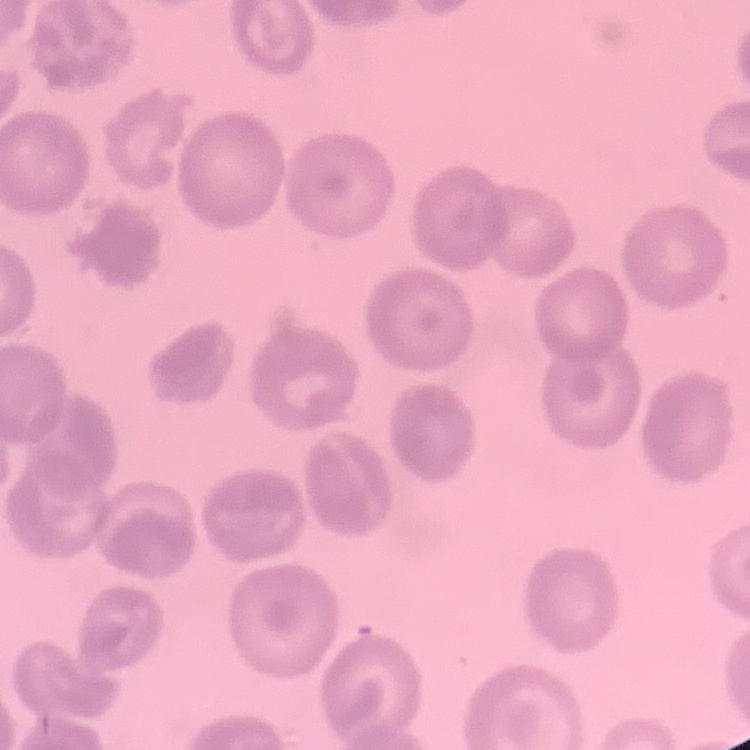
red_blood_cell_morphology: no rouleaux formation
stain: Field's or Giemsa
preparation: thin blood smear
image_type: one tile cut from a larger photomicrograph